Locate and identify every blood parasite.
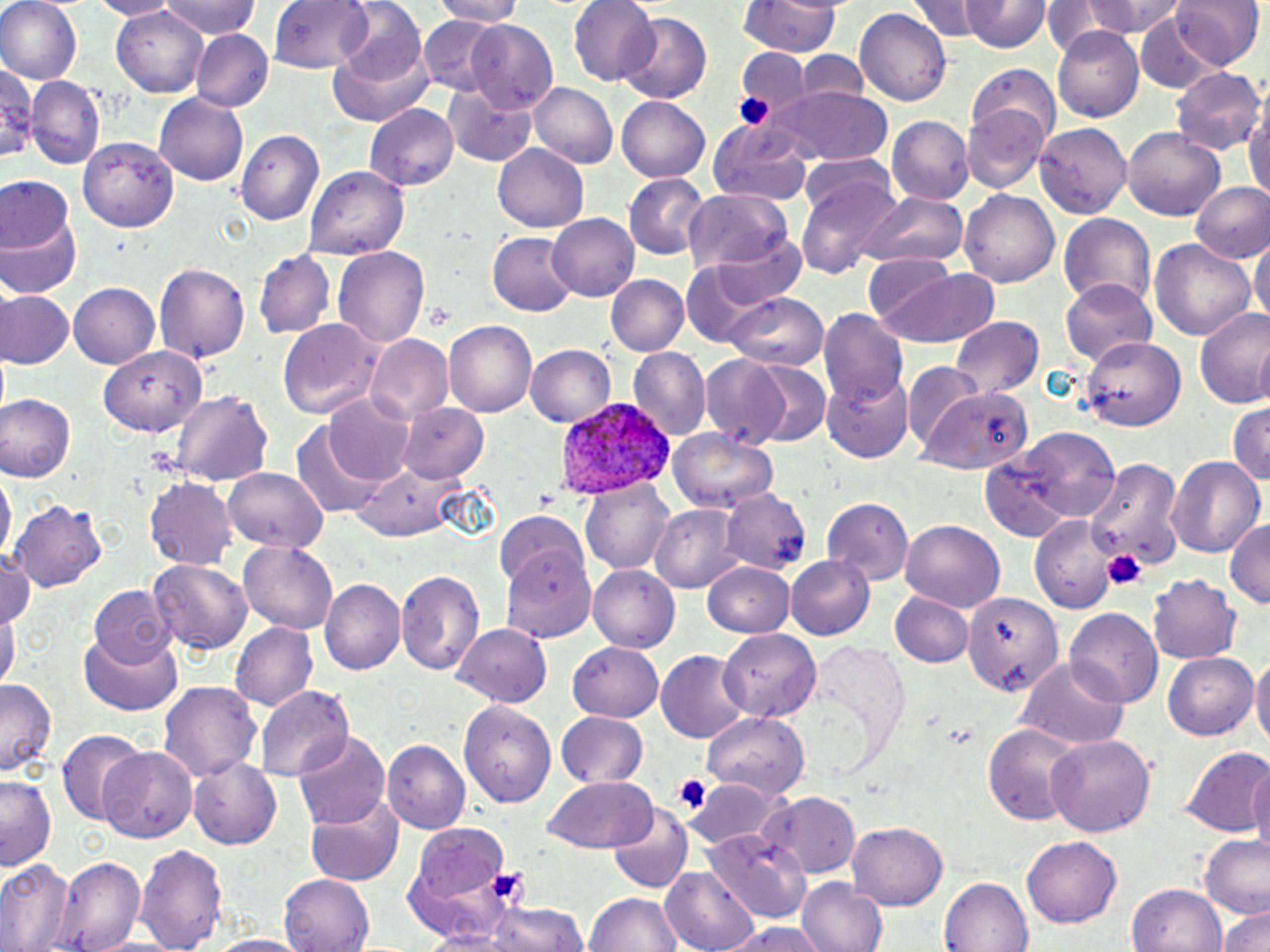
Approximate bounding boxes as (x1,y1)-(x2,y2) corner pairs in pixels.
Plasmodium ovale-infected red blood cells: (557,398)-(673,501).
No Plasmodium falciparum, Plasmodium malariae, Plasmodium vivax, Babesia divergens, or Trypanosoma brucei observed.

Summary:
  - Uninfected red blood cell locations: (0,0)-(82,85), (86,0)-(179,20), (157,0)-(261,40), (271,0)-(376,75), (434,0)-(529,26), (569,0)-(659,86), (738,0)-(844,57), (913,0)-(983,41), (1052,0)-(1192,41), (1174,0)-(1264,72), (965,1)-(1049,54), (331,2)-(428,85), (111,5)-(210,95), (856,7)-(952,110), (616,12)-(714,104), (1133,13)-(1223,94), (419,15)-(508,97), (467,21)-(558,112), (325,26)-(432,129), (1053,26)-(1145,123), (192,29)-(273,113), (734,49)-(810,126), (795,51)-(871,106), (965,66)-(1062,147), (1172,68)-(1264,155), (28,76)-(106,170), (444,81)-(539,167), (529,82)-(617,168), (773,90)-(892,165), (1244,92)-(1270,207), (153,94)-(248,187), (615,97)-(711,181), (365,104)-(459,192), (962,106)-(1050,196), (888,115)-(974,205), (709,117)-(815,206), (1035,125)-(1133,216), (1122,128)-(1226,219), (237,129)-(325,226), (79,134)-(183,229), (492,144)-(587,232), (305,167)-(410,257), (796,171)-(905,280), (623,172)-(708,261), (0,178)-(74,254), (1189,180)-(1270,262), (959,187)-(1061,286), (682,190)-(793,277), (860,192)-(967,269), (1057,211)-(1155,308), (548,214)-(639,302), (0,217)-(81,300), (705,229)-(808,308), (487,231)-(578,316), (1252,236)-(1268,329), (1151,238)-(1256,341), (333,245)-(430,348), (254,250)-(335,340), (679,254)-(796,344), (866,254)-(961,335), (153,263)-(249,364), (883,267)-(1002,348), (604,274)-(687,356), (1057,276)-(1158,368), (70,282)-(162,368), (1,290)-(73,370), (720,294)-(829,371), (1194,306)-(1270,412), (819,309)-(909,412), (949,316)-(1043,401), (277,319)-(381,418), (445,320)-(539,418), (365,335)-(453,425), (1083,337)-(1184,430), (526,345)-(618,429), (100,347)-(205,440), (629,347)-(710,439), (700,354)-(792,448), (742,361)-(832,449), (904,364)-(986,455), (822,374)-(913,462), (921,387)-(1035,477), (166,390)-(275,486), (0,393)-(76,482), (325,394)-(417,486), (398,400)-(488,481), (1227,400)-(1270,486), (290,422)-(392,520), (668,428)-(778,512), (1004,429)-(1124,525), (981,455)-(1072,540), (1166,455)-(1265,559), (1088,460)-(1184,572), (351,464)-(465,542), (223,467)-(329,551), (0,472)-(13,565), (146,477)-(235,568), (581,480)-(671,575), (722,489)-(809,574), (821,495)-(913,583), (13,501)-(105,593), (653,503)-(744,594), (495,508)-(593,594), (1029,515)-(1122,613), (898,520)-(1005,611), (1224,520)-(1270,612), (239,540)-(338,632), (0,554)-(37,630), (785,554)-(875,639), (502,558)-(597,642), (148,560)-(252,655), (704,560)-(795,636), (588,565)-(681,651), (396,570)-(484,677), (1150,576)-(1244,663), (322,579)-(403,676), (90,587)-(176,667), (892,591)-(971,667), (961,591)-(1061,698), (1,606)-(18,693), (1067,608)-(1160,706), (231,623)-(318,711), (454,623)-(551,706), (717,629)-(822,720), (78,631)-(183,715), (804,639)-(909,766), (568,641)-(662,719), (656,651)-(749,745), (1161,653)-(1256,740), (1252,655)-(1270,756), (1016,658)-(1129,749), (0,681)-(56,776), (159,682)-(261,783), (256,684)-(355,781), (460,699)-(560,805), (556,711)-(648,788), (703,713)-(809,802), (982,724)-(1081,824), (296,730)-(389,828), (57,731)-(145,823), (1045,733)-(1155,835), (384,741)-(469,834), (1181,744)-(1268,838), (99,745)-(197,843), (1245,755)-(1270,853), (188,758)-(284,848), (1,775)-(58,871), (544,776)-(660,854), (688,780)-(778,852), (303,792)-(404,887), (760,793)-(861,878), (608,807)-(692,893), (848,822)-(947,910), (406,824)-(509,921), (702,828)-(808,922), (1198,835)-(1270,917), (1023,836)-(1121,926), (139,840)-(227,952), (52,856)-(147,951), (0,858)-(73,952), (664,864)-(763,952), (280,874)-(372,952), (940,875)-(1032,952), (799,876)-(887,952), (1128,884)-(1228,952), (586,892)-(683,952), (438,899)-(594,952), (1217,905)-(1270,952), (719,922)-(827,952), (202,932)-(306,952)
  - Platelet locations: (734,91)-(779,135), (1102,548)-(1147,589), (669,774)-(712,815)
  - Slide-level diagnosis: Plasmodium ovale
  - Preparation: thin blood smear
  - Magnification: 1000x
  - Field of view: single
  - Image size: 1270×952 pixels
  - Stain: May-Grünwald-Giemsa
  - Modality: optical microscopy